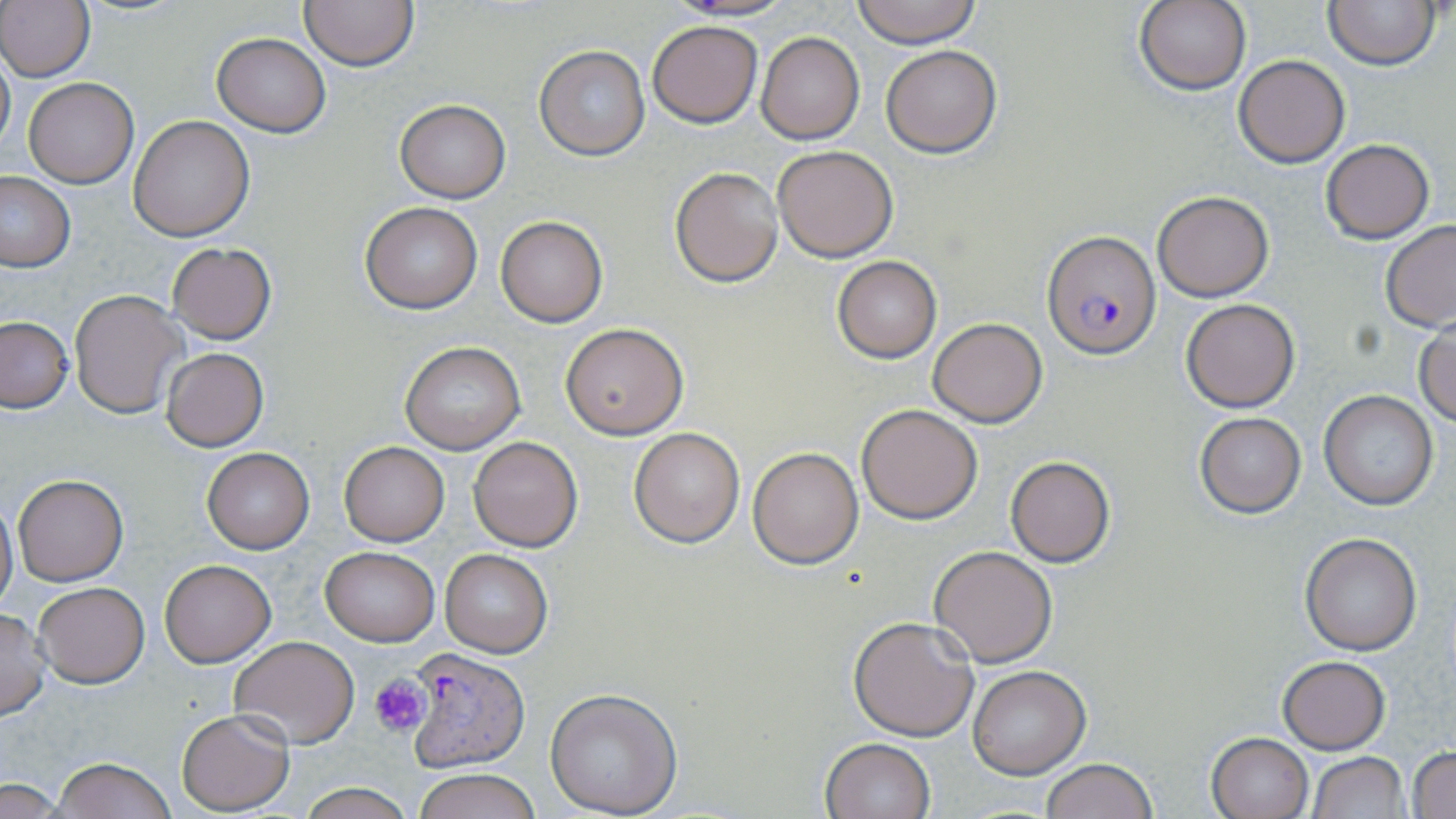
slide_level_diagnosis: Plasmodium falciparum
modality: light microscopy
preparation: thin blood film
plasmodium_falciparum_infected_red_blood_cell_locations: 'approximate bounding boxes as named x1/y1/x2/y2 corners in pixels: (x1=1043, y1=231, x2=1159, y2=358), (x1=407, y1=647, x2=532, y2=776)'
field_of_view: single
magnification: 1000x
image_size: 1456×819 pixels
platelet_locations: 'approximate bounding boxes as named x1/y1/x2/y2 corners in pixels: (x1=370, y1=674, x2=430, y2=739)'
stain: May-Grünwald-Giemsa
uninfected_red_blood_cell_locations: 'approximate bounding boxes as named x1/y1/x2/y2 corners in pixels: (x1=0, y1=0, x2=95, y2=83), (x1=298, y1=0, x2=419, y2=71), (x1=669, y1=0, x2=796, y2=21), (x1=850, y1=0, x2=983, y2=47), (x1=1135, y1=0, x2=1253, y2=96), (x1=1323, y1=0, x2=1440, y2=70), (x1=648, y1=20, x2=762, y2=128), (x1=755, y1=30, x2=865, y2=145), (x1=212, y1=33, x2=330, y2=137), (x1=0, y1=45, x2=15, y2=157), (x1=881, y1=45, x2=1002, y2=157), (x1=533, y1=46, x2=650, y2=161), (x1=1234, y1=55, x2=1350, y2=167), (x1=22, y1=78, x2=139, y2=187), (x1=394, y1=100, x2=510, y2=202), (x1=128, y1=116, x2=254, y2=240), (x1=1320, y1=138, x2=1436, y2=243), (x1=772, y1=146, x2=899, y2=262), (x1=670, y1=166, x2=784, y2=286), (x1=0, y1=172, x2=75, y2=272), (x1=1151, y1=190, x2=1274, y2=302), (x1=360, y1=203, x2=483, y2=313), (x1=494, y1=214, x2=608, y2=328), (x1=1379, y1=220, x2=1456, y2=331), (x1=167, y1=243, x2=277, y2=345), (x1=832, y1=255, x2=942, y2=363), (x1=69, y1=290, x2=187, y2=419), (x1=1181, y1=299, x2=1299, y2=412), (x1=0, y1=317, x2=74, y2=412), (x1=928, y1=317, x2=1048, y2=427), (x1=560, y1=322, x2=689, y2=440), (x1=1414, y1=322, x2=1456, y2=427), (x1=399, y1=342, x2=526, y2=454), (x1=161, y1=348, x2=268, y2=451), (x1=1319, y1=390, x2=1439, y2=510), (x1=856, y1=403, x2=983, y2=523), (x1=1193, y1=412, x2=1306, y2=518), (x1=628, y1=427, x2=746, y2=547), (x1=467, y1=435, x2=583, y2=552), (x1=339, y1=441, x2=449, y2=546), (x1=748, y1=447, x2=862, y2=568), (x1=202, y1=448, x2=314, y2=554), (x1=1005, y1=457, x2=1115, y2=566), (x1=12, y1=474, x2=127, y2=586), (x1=0, y1=495, x2=17, y2=614), (x1=1301, y1=533, x2=1422, y2=656), (x1=929, y1=545, x2=1058, y2=666), (x1=320, y1=547, x2=439, y2=645), (x1=440, y1=548, x2=553, y2=658), (x1=160, y1=559, x2=276, y2=667), (x1=34, y1=583, x2=148, y2=687), (x1=0, y1=607, x2=51, y2=720), (x1=848, y1=615, x2=980, y2=741), (x1=229, y1=636, x2=360, y2=749), (x1=1277, y1=655, x2=1389, y2=755), (x1=967, y1=665, x2=1091, y2=778), (x1=544, y1=686, x2=683, y2=816), (x1=175, y1=710, x2=295, y2=813), (x1=1205, y1=732, x2=1312, y2=819), (x1=820, y1=737, x2=936, y2=819), (x1=1409, y1=747, x2=1455, y2=817), (x1=1306, y1=752, x2=1409, y2=818), (x1=54, y1=758, x2=178, y2=818), (x1=1041, y1=758, x2=1158, y2=819), (x1=414, y1=768, x2=540, y2=819), (x1=1, y1=779, x2=63, y2=816), (x1=295, y1=781, x2=417, y2=818)'